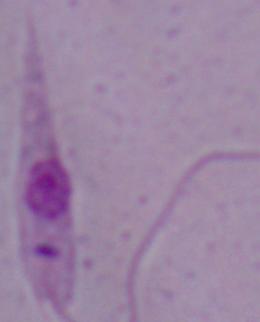

Summary:
  - Identification: Leishmania
  - Magnification: 1000x
  - Modality: micrograph